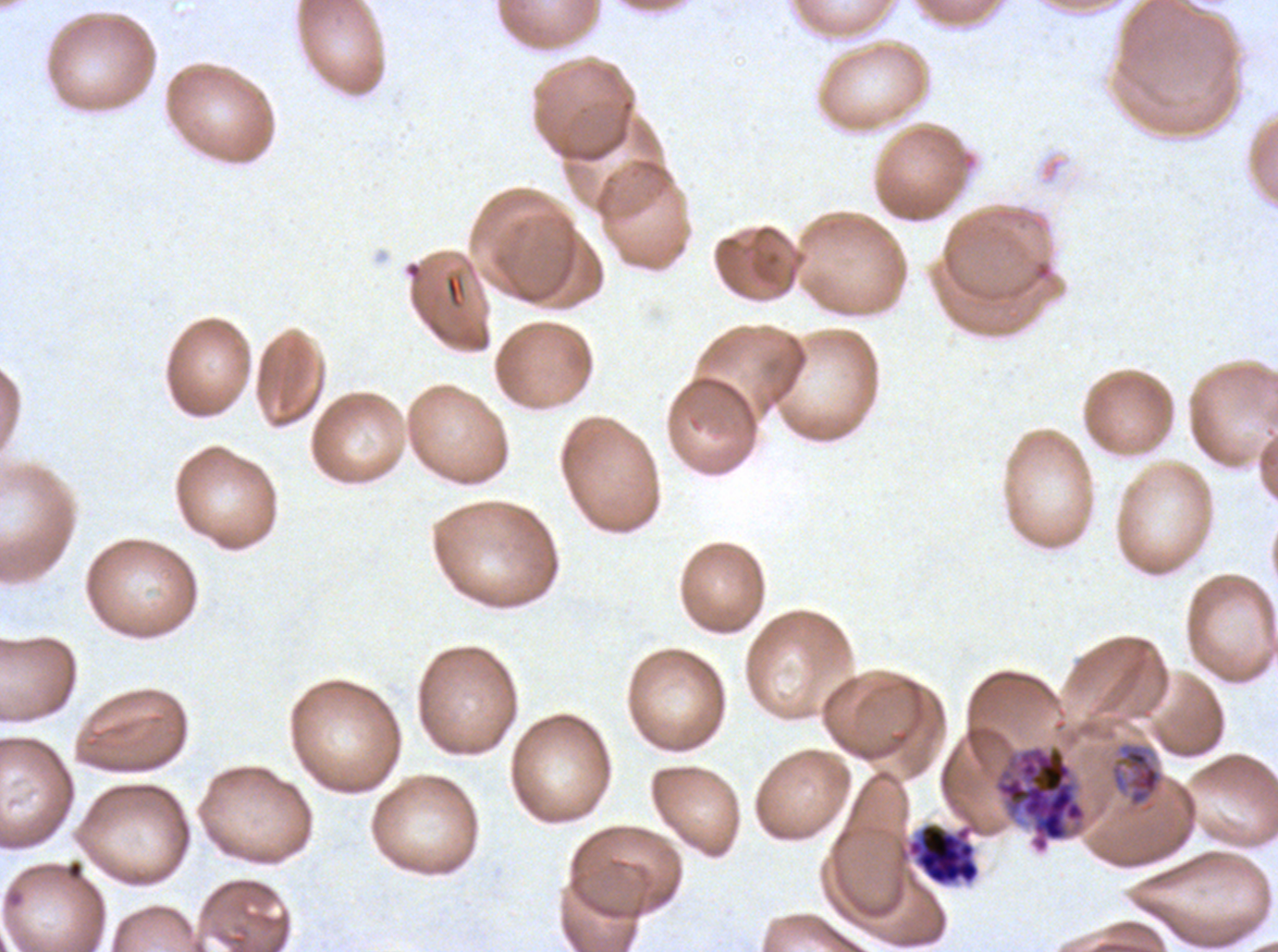

Approximate bounding boxes as (x1, y1, x2, y2) in pixels.
Summary:
  - Mid trophozoite locations: (1110, 742, 1162, 808)
  - Segmenter locations: (992, 744, 1088, 854), (906, 822, 980, 886)
  - Field of view: one sub-image of a larger composite
  - Stain: Giemsa
  - Specimen: P. falciparum from a patient in The Gambia, cultured ex vivo for 24 to 48 hours
  - Preparation: thin blood smear
  - Image size: 1278×952 pixels
  - Life-cycle stages observed: mid trophozoite, segmenter